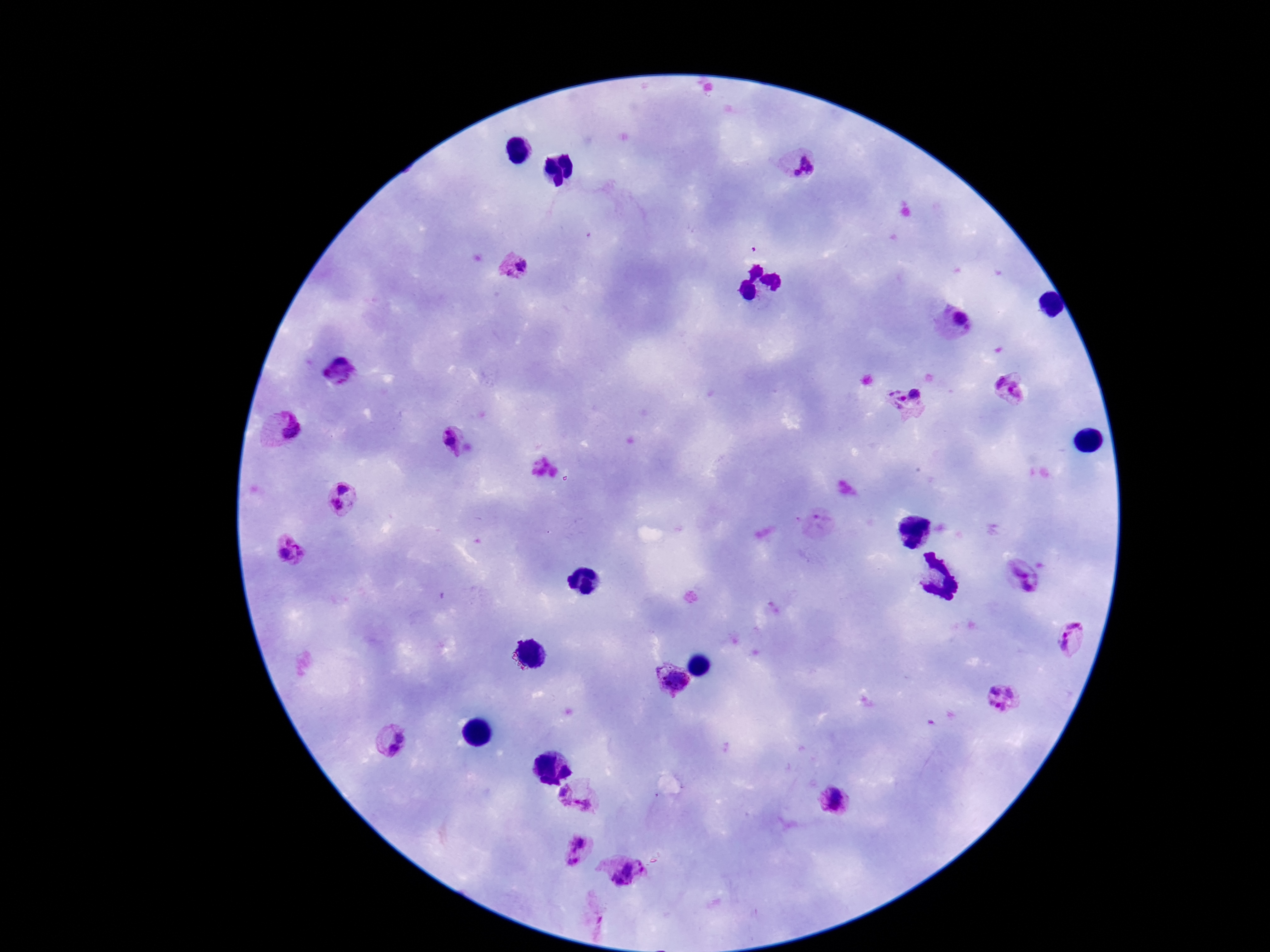

Approximate centers as {x, y} in pixels. Plasmodium parasite locations: {798, 162}, {513, 266}, {954, 320}, {339, 373}, {1011, 386}, {906, 400}, {279, 428}, {460, 442}, {343, 488}, {336, 504}, {820, 524}, {288, 551}, {1021, 575}, {1072, 639}, {672, 682}, {1003, 698}, {389, 738}, {576, 797}, {837, 801}, {584, 850}, {624, 872}. Image is 1270×952 pixels. Giemsa stain. Smartphone photograph taken through the microscope eyepiece. Patient malaria status: positive. Single field of view. Thick blood smear. 100x magnification.